Assess this cell for malaria.
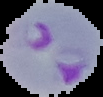

It is parasitized.

Summary:
  - Image size: 103×97 pixels
  - Image type: segmented cell region on a black background
  - Preparation: thin blood smear